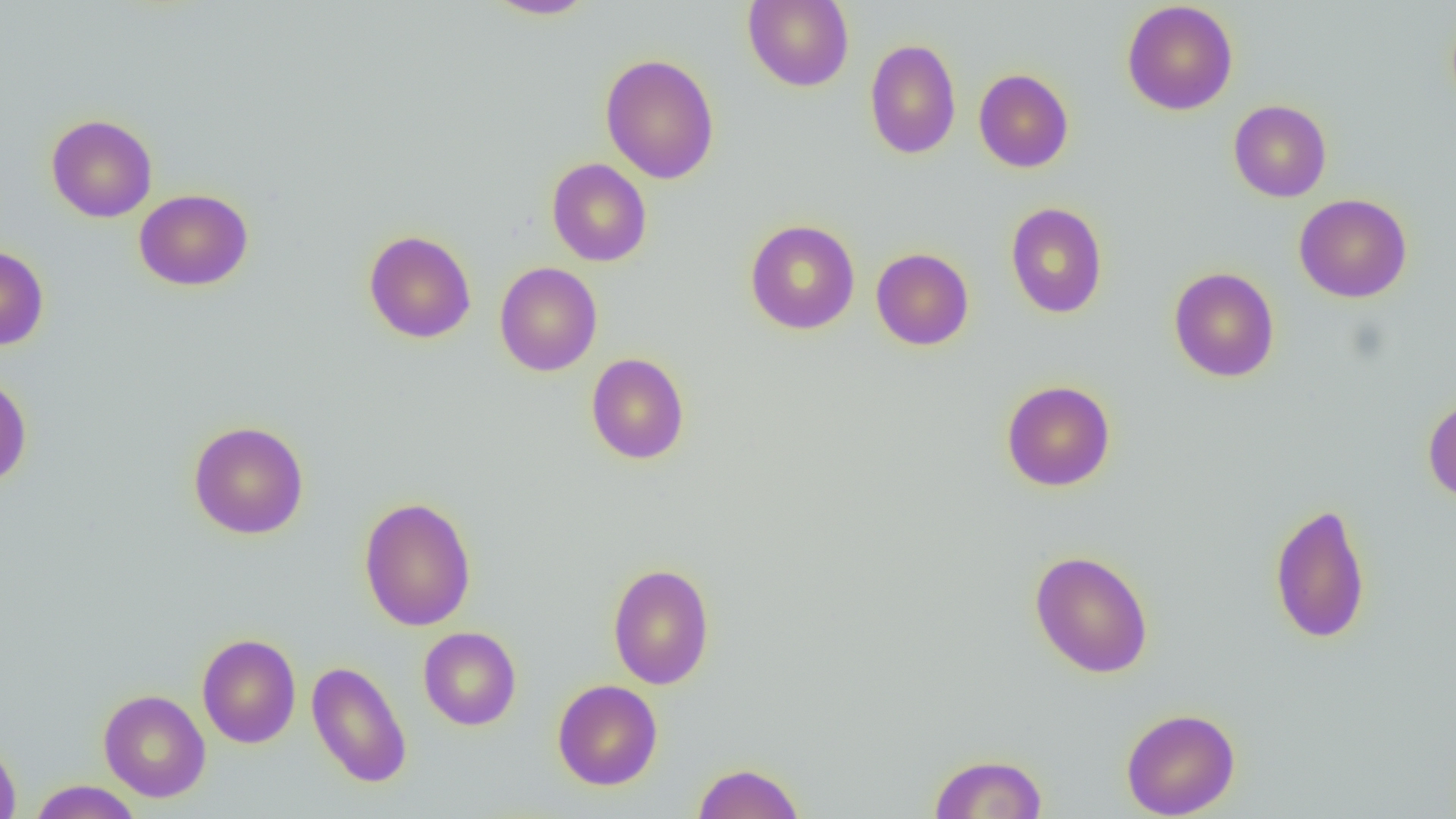

slide_level_diagnosis: no evidence of blood parasites
magnification: 1000x
field_of_view: one of a larger specimen
modality: optical microscopy
image_size: 1456×819 pixels
preparation: thin blood film
uninfected_red_blood_cell_locations: 'approximate bounding boxes as [x1, y1, x2, y2] in pixels: [483, 0, 597, 19], [742, 0, 854, 92], [1121, 1, 1238, 116], [865, 38, 961, 159], [599, 53, 720, 184], [973, 68, 1074, 173], [1228, 99, 1332, 202], [46, 113, 158, 222], [546, 158, 652, 266], [134, 188, 253, 291], [1294, 193, 1412, 303], [1005, 202, 1108, 318], [745, 219, 860, 334], [363, 229, 476, 343], [0, 243, 49, 351], [871, 248, 974, 350], [494, 262, 602, 376], [1168, 267, 1280, 382], [586, 353, 690, 465], [0, 373, 32, 488], [1001, 380, 1116, 492], [1423, 395, 1456, 503], [188, 421, 309, 539], [359, 496, 477, 631], [1269, 500, 1371, 645], [1029, 550, 1154, 678], [607, 563, 715, 689], [418, 626, 521, 730], [197, 633, 301, 749], [306, 660, 412, 788], [552, 679, 663, 790], [98, 689, 211, 802], [1121, 707, 1241, 818], [0, 736, 21, 819], [929, 753, 1048, 818], [692, 762, 805, 819], [28, 780, 144, 818]'